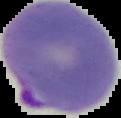

Summary:
  - Malaria status: parasitized
  - Image type: segmented cell region with the area outside set to black
  - Image size: 121×118 pixels
  - Preparation: thin blood film